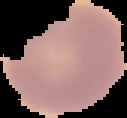

Summary:
  - Preparation: thin blood smear
  - Image size: 127×118 pixels
  - Malaria status: uninfected
  - Image type: segmented cell region on a black background